Assess for malaria.
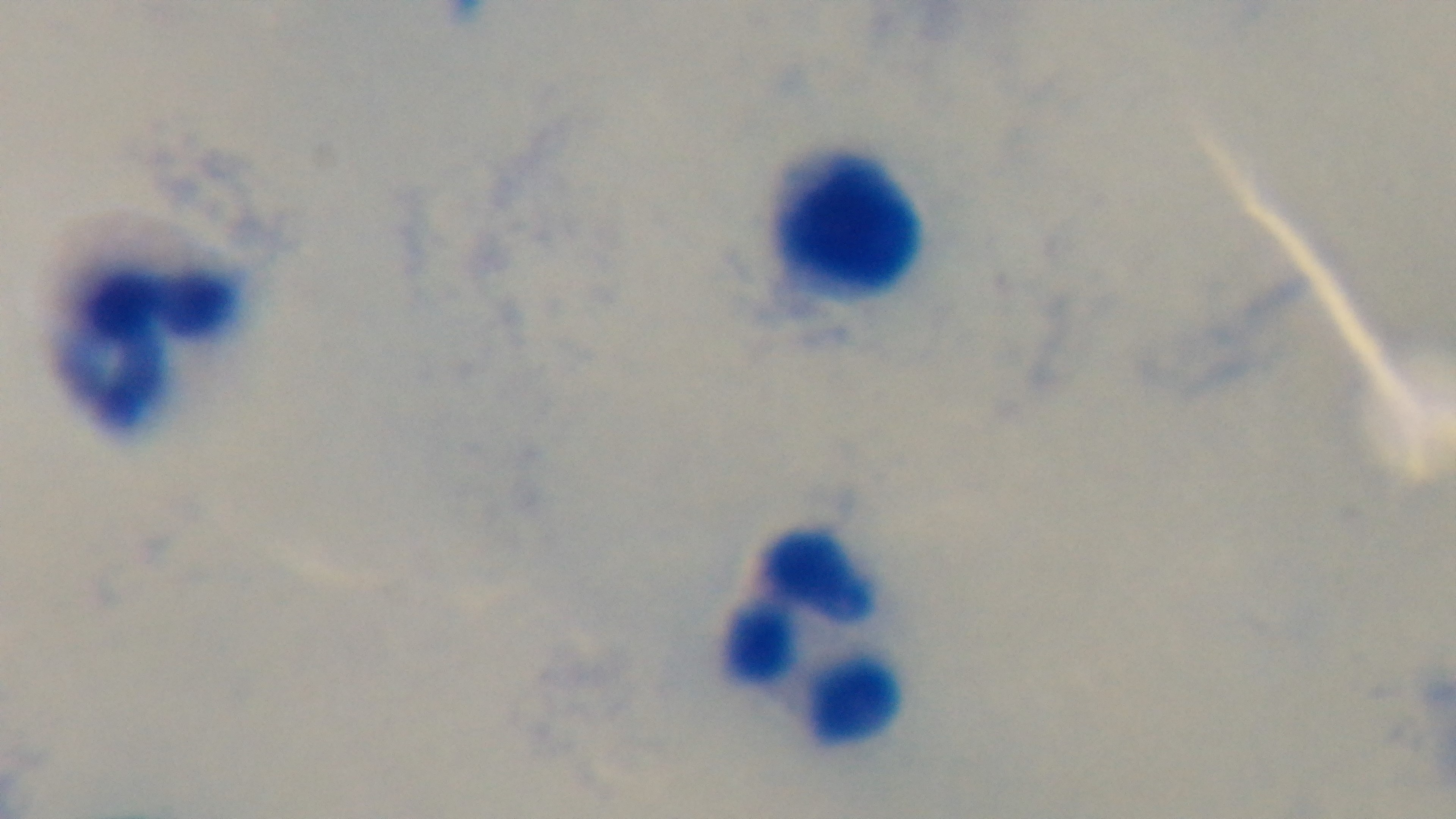

Negative.

One field from the slide. Mounted 4K digital camera. 100x oil-immersion objective. Preparation: thick smear. Giemsa-stained. Photomicrograph.